Report the malaria status of this cell.
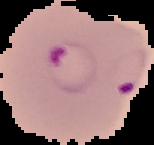

It is parasitized.

Summary:
  - Preparation: thin blood film
  - Image type: segmented cell region on a black background
  - Image size: 154×145 pixels